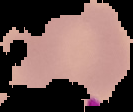

Summary:
  - Malaria status: uninfected
  - Preparation: thin blood film
  - Image size: 133×112 pixels
  - Image type: segmented cell region on a black background